Classify this cell by malaria status.
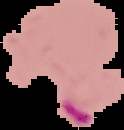

It is parasitized.

Image is 124×130 pixels. Segmented cell region on a black background. From a thin blood smear.